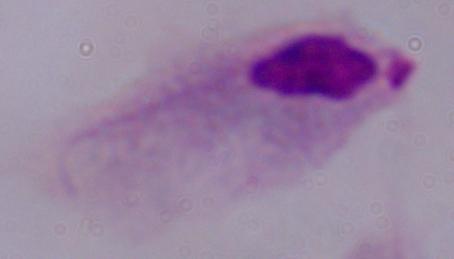 Photomicrograph. A trichomonad is shown. Captured at 1000x magnification.